Give the position of every leukocyte visible.
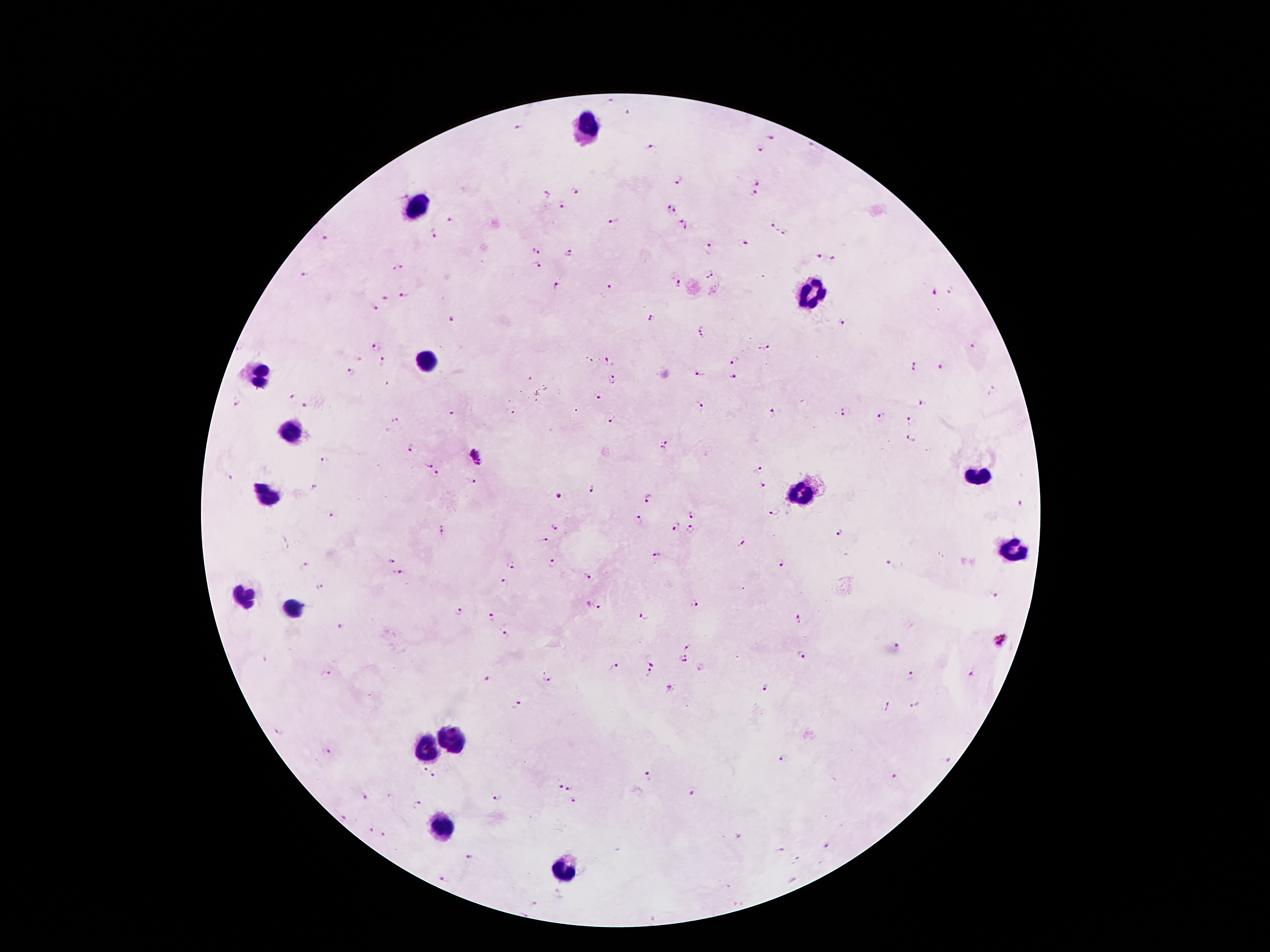
Approximate centers as {x, y} in pixels.
Leukocytes: {590, 128}, {422, 207}, {811, 291}, {429, 356}, {259, 371}, {295, 429}, {979, 479}, {799, 493}, {264, 495}, {1015, 551}, {242, 599}, {290, 608}, {453, 740}, {427, 750}, {447, 827}, {557, 872}.

Malaria parasite locations: {606, 103}, {516, 127}, {771, 136}, {650, 147}, {808, 147}, {759, 149}, {677, 180}, {758, 182}, {574, 191}, {547, 193}, {752, 194}, {401, 196}, {561, 204}, {671, 210}, {614, 219}, {450, 221}, {685, 224}, {773, 224}, {432, 234}, {786, 234}, {324, 238}, {743, 244}, {709, 249}, {536, 250}, {569, 253}, {818, 258}, {832, 259}, {534, 264}, {397, 268}, {708, 272}, {304, 274}, {678, 283}, {556, 287}, {611, 288}, {935, 290}, {949, 292}, {405, 295}, {383, 296}, {375, 308}, {651, 318}, {454, 320}, {839, 322}, {702, 325}, {702, 338}, {974, 345}, {377, 346}, {764, 347}, {606, 360}, {734, 360}, {383, 363}, {941, 366}, {914, 367}, {351, 372}, {699, 374}, {733, 377}, {530, 379}, {613, 381}, {991, 391}, {596, 397}, {292, 398}, {236, 402}, {920, 402}, {306, 405}, {699, 408}, {845, 412}, {452, 414}, {773, 414}, {881, 416}, {394, 418}, {612, 419}, {909, 421}, {910, 439}, {665, 444}, {410, 448}, {477, 456}, {326, 460}, {430, 465}, {759, 467}, {436, 474}, {229, 475}, {472, 480}, {762, 485}, {315, 487}, {591, 488}, {558, 495}, {647, 499}, {1019, 502}, {775, 510}, {331, 515}, {691, 515}, {638, 520}, {675, 527}, {441, 528}, {554, 528}, {689, 528}, {839, 531}, {543, 541}, {740, 541}, {656, 552}, {390, 561}, {551, 563}, {781, 564}, {889, 565}, {305, 566}, {509, 567}, {397, 572}, {587, 574}, {504, 584}, {320, 586}, {996, 598}, {695, 601}, {598, 606}, {459, 612}, {490, 616}, {644, 616}, {797, 618}, {339, 625}, {504, 634}, {1002, 640}, {688, 646}, {897, 647}, {803, 655}, {685, 660}, {650, 661}, {614, 667}, {649, 672}, {326, 673}, {548, 675}, {972, 675}, {911, 677}, {485, 678}, {766, 687}, {670, 690}, {516, 703}, {915, 704}, {887, 705}, {279, 731}, {327, 752}, {783, 759}, {947, 759}, {424, 769}, {893, 775}, {432, 776}, {648, 776}, {558, 784}, {571, 788}, {690, 790}, {364, 797}, {497, 797}, {572, 801}, {417, 805}, {344, 817}, {370, 828}, {384, 834}, {736, 836}, {827, 844}, {781, 850}, {468, 856}, {443, 878}, {534, 903}, {524, 915}. Thick blood smear. Image is 1270×952 pixels. Smartphone photograph taken through the microscope eyepiece. One field from this slide. 100x magnification. Patient malaria status: positive for Plasmodium falciparum. Giemsa-stained preparation.